Name the parasite shown.
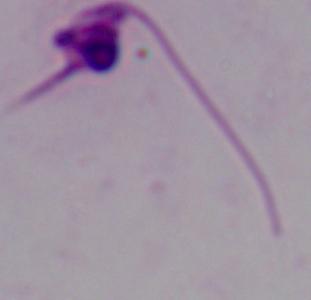

This is Leishmania.

Micrograph. 1000x magnification.